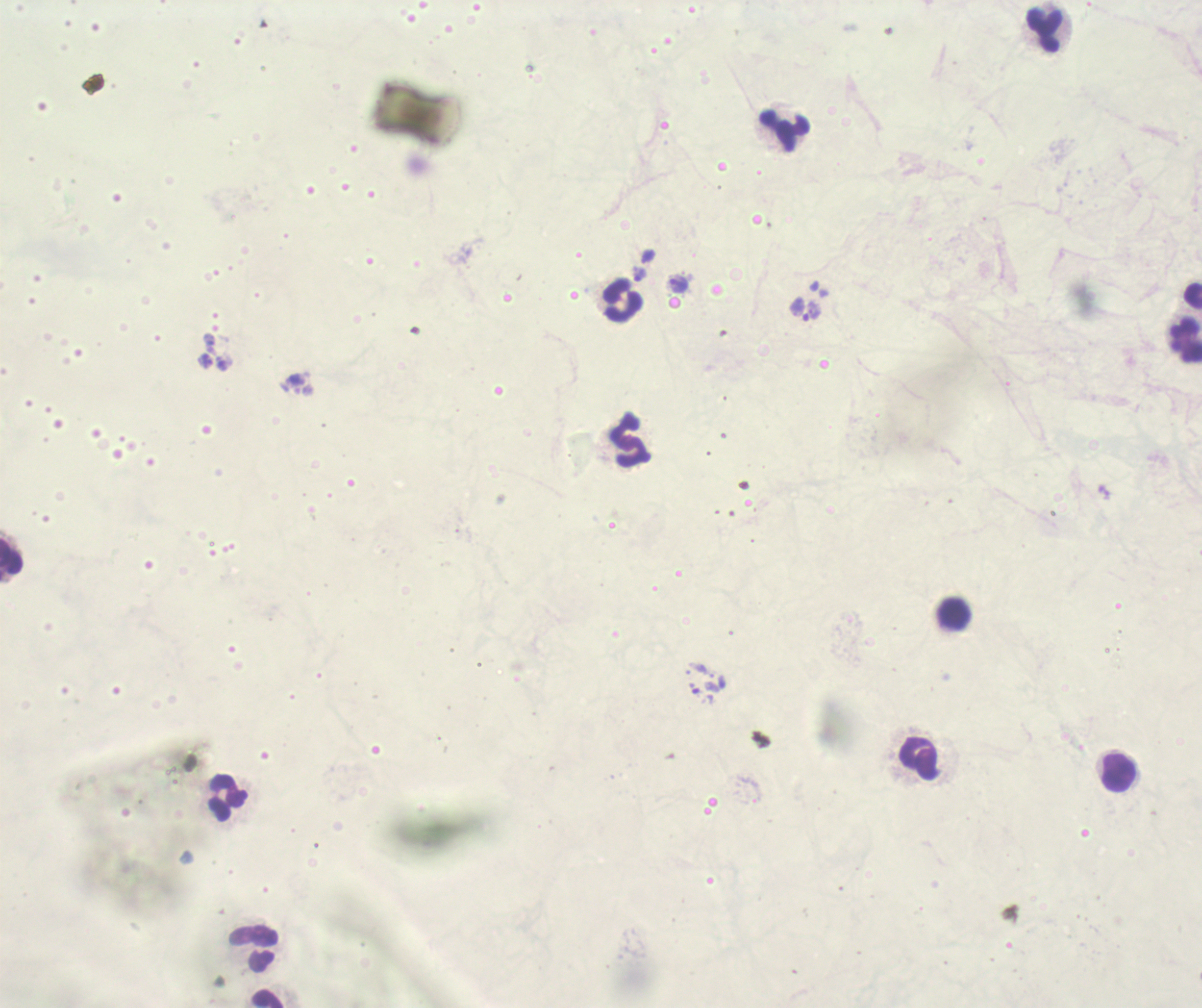
{
  "background_quality": "unsatisfactory",
  "magnification": "100x",
  "stain": "Romanowsky",
  "coloration_quality": "bad",
  "image_size": "1202×1008 pixels",
  "preparation": "thick blood smear",
  "leukocyte_locations": "approximate centers as (x, y) in pixels: (1044, 28), (784, 130), (619, 299), (1185, 341), (630, 440), (12, 556), (954, 613), (918, 757), (1119, 772), (225, 798), (254, 950), (267, 998)",
  "result": "malaria parasites detected",
  "field_of_view": "single",
  "context": "previously used in an actual diagnosis",
  "trophozoite_locations": "approximate centers as (x, y) in pixels: (677, 284), (806, 310)"
}